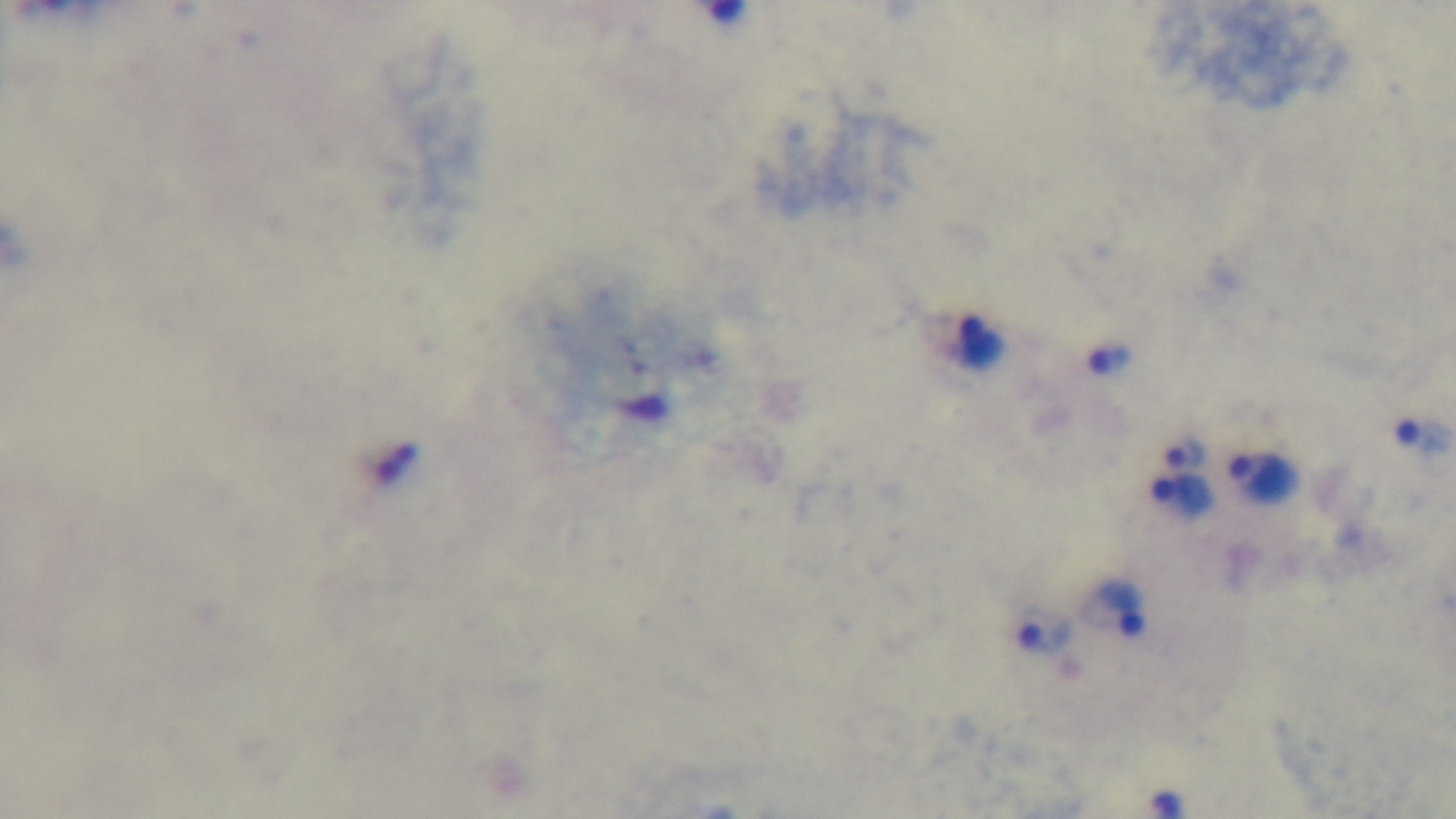
Malaria status: positive. Light microscopy. Preparation: thick smear. One field from the slide. Giemsa stain. Mounted 4K digital camera. 100x oil-immersion objective.